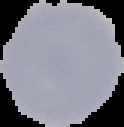 Image is 124×127 pixels. From a thin blood film. Cell region segmented out of the field of view; the surrounding area is masked to black. Result: no Plasmodium parasites seen.